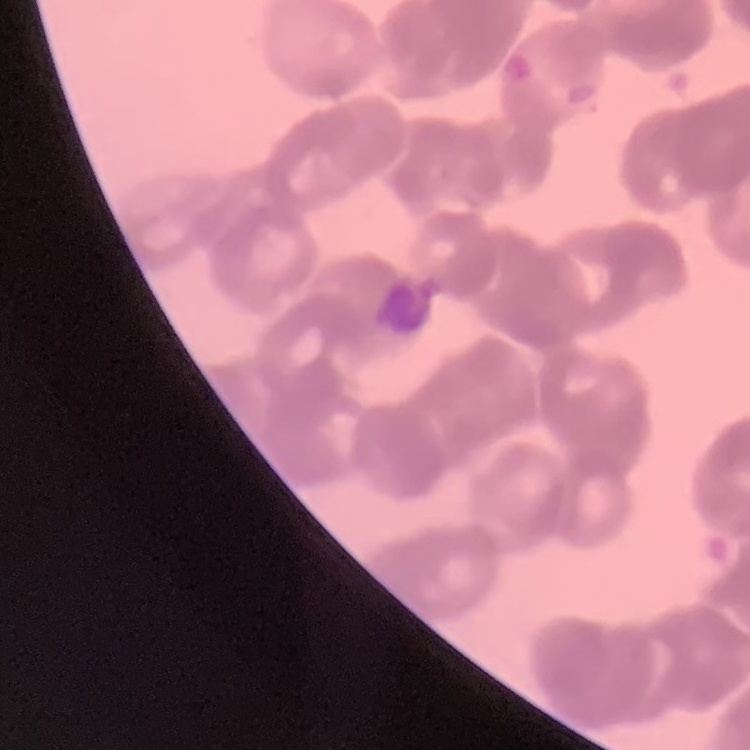

The erythrocytes show rouleaux formation. Square crop of a larger photomicrograph. Field's or Giemsa stain. Thin blood smear.